Outline each blood parasite and name the species.
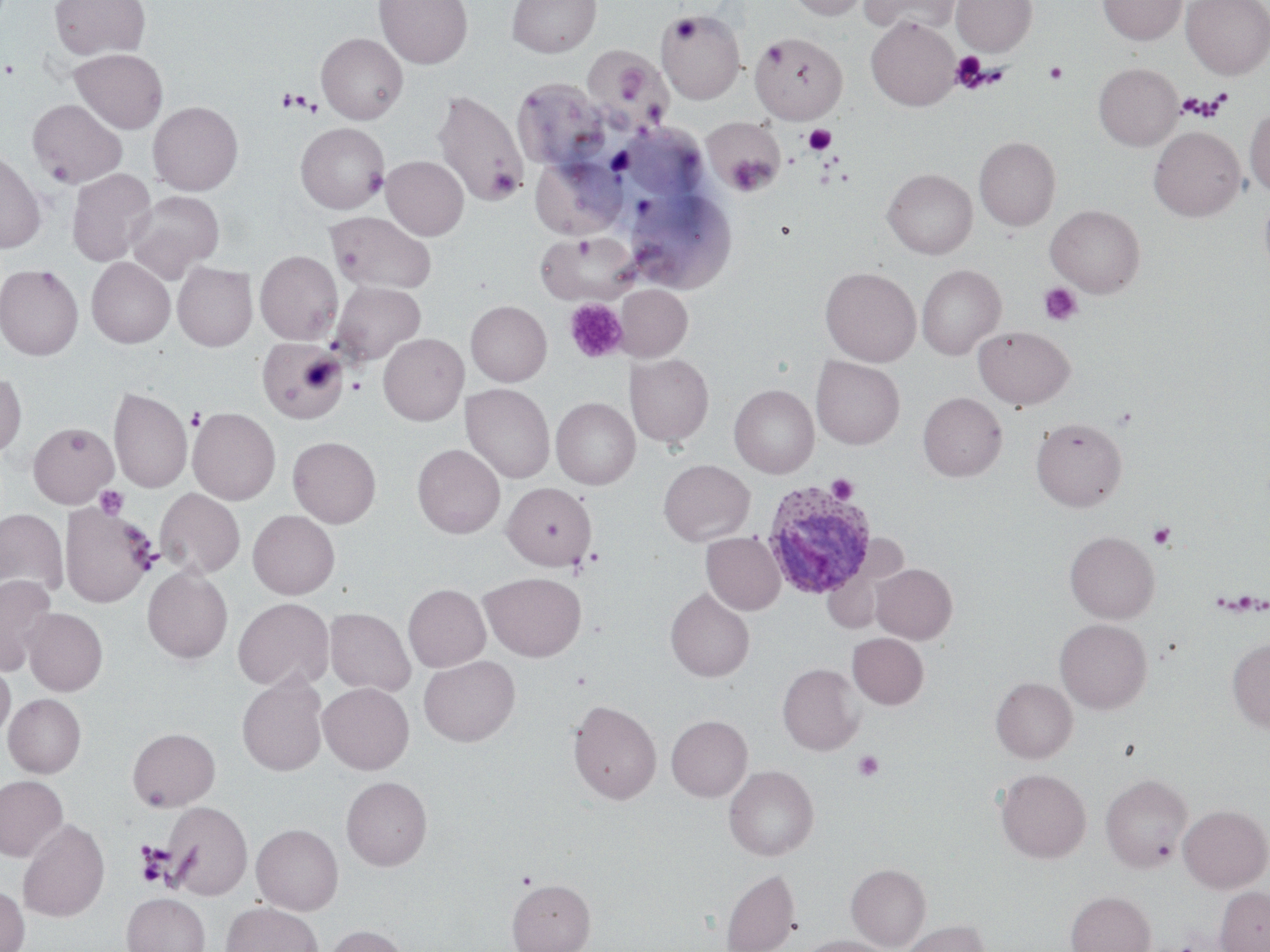

Approximate bounding boxes as (x1,y1)-(x2,y2) corner pairs in pixels.
Plasmodium ovale-infected red blood cells: (761,479)-(876,600).
No Plasmodium falciparum, Plasmodium malariae, Plasmodium vivax, Babesia divergens, or Trypanosoma brucei observed.

Platelet locations: (669,16)-(702,43), (762,39)-(788,69), (950,51)-(988,91), (610,61)-(648,105), (1045,62)-(1067,84), (280,88)-(305,112), (290,94)-(316,115), (804,125)-(837,154), (726,155)-(774,196), (362,166)-(387,197), (488,169)-(523,199), (1040,282)-(1082,326), (564,298)-(628,363), (348,378)-(365,395), (186,407)-(205,430), (826,475)-(859,502), (94,485)-(129,520), (1148,523)-(1177,549), (583,548)-(604,570), (571,550)-(599,576), (853,750)-(884,781), (135,843)-(176,887). Uninfected red blood cell locations: (49,0)-(150,60), (375,0)-(473,68), (507,0)-(601,57), (786,0)-(870,20), (861,0)-(960,35), (951,0)-(1037,56), (1098,0)-(1186,45), (1182,0)-(1270,79), (656,9)-(745,103), (866,16)-(960,111), (316,32)-(408,124), (750,32)-(848,124), (71,48)-(168,133), (590,52)-(660,115), (1093,63)-(1183,151), (513,77)-(611,172), (433,91)-(526,205), (27,99)-(127,188), (148,101)-(243,195), (1245,107)-(1270,196), (702,115)-(785,196), (296,123)-(389,213), (1149,127)-(1245,221), (974,136)-(1061,231), (0,148)-(46,254), (382,156)-(468,240), (532,156)-(626,239), (67,168)-(157,267), (882,168)-(977,259), (620,184)-(734,293), (1259,190)-(1270,281), (127,191)-(224,281), (1046,205)-(1145,297), (327,211)-(436,293), (537,233)-(639,305), (255,250)-(342,344), (86,257)-(175,348), (173,262)-(257,351), (917,264)-(1005,359), (0,265)-(83,360), (820,267)-(921,366), (331,282)-(425,365), (615,284)-(692,361), (466,300)-(551,386), (973,326)-(1075,409), (378,333)-(468,425), (257,338)-(348,423), (625,354)-(713,447), (812,357)-(904,449), (0,369)-(27,459), (461,383)-(554,484), (729,384)-(819,477), (108,386)-(192,493), (918,392)-(1006,481), (551,397)-(640,489), (188,407)-(280,505), (1031,417)-(1127,511), (27,422)-(119,508), (288,436)-(381,528), (412,444)-(505,539), (659,459)-(755,546), (502,482)-(596,570), (155,488)-(245,579), (59,502)-(157,607), (0,508)-(68,601), (248,510)-(339,599), (1065,530)-(1159,623), (702,532)-(785,615), (871,564)-(957,643), (143,567)-(233,663), (823,568)-(882,633), (480,572)-(586,661), (0,575)-(57,674), (403,583)-(490,672), (665,588)-(754,682), (233,597)-(334,691), (324,607)-(415,696), (23,608)-(108,695), (1055,618)-(1152,714), (847,633)-(928,709), (1227,638)-(1270,732), (419,655)-(520,746), (0,661)-(15,741), (778,663)-(863,755), (237,674)-(328,776), (991,677)-(1077,762), (318,682)-(414,774), (4,693)-(86,777), (567,699)-(662,805), (666,715)-(752,801), (127,727)-(220,810), (724,765)-(819,860), (996,769)-(1091,863), (1101,774)-(1192,871), (0,775)-(68,862), (341,776)-(432,870), (163,801)-(253,900), (1179,804)-(1270,892), (17,818)-(109,922), (251,823)-(343,915), (846,863)-(931,950), (720,869)-(801,952), (507,878)-(595,952), (0,886)-(30,952), (1215,887)-(1270,952), (1066,890)-(1155,952), (122,892)-(210,952), (221,902)-(323,952), (900,919)-(989,952), (323,925)-(410,952), (799,936)-(893,952). Slide-level diagnosis: Plasmodium ovale. 1000x magnification. Single field of view. Light microscopy. Image is 1270×952 pixels. Thin blood film. May-Grünwald-Giemsa-stained preparation.